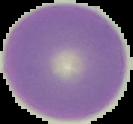 Image is 133×124 pixels. Result: no Plasmodium parasites detected. Segmented cell region on a black background. From a thin blood film.